Assess the background quality.
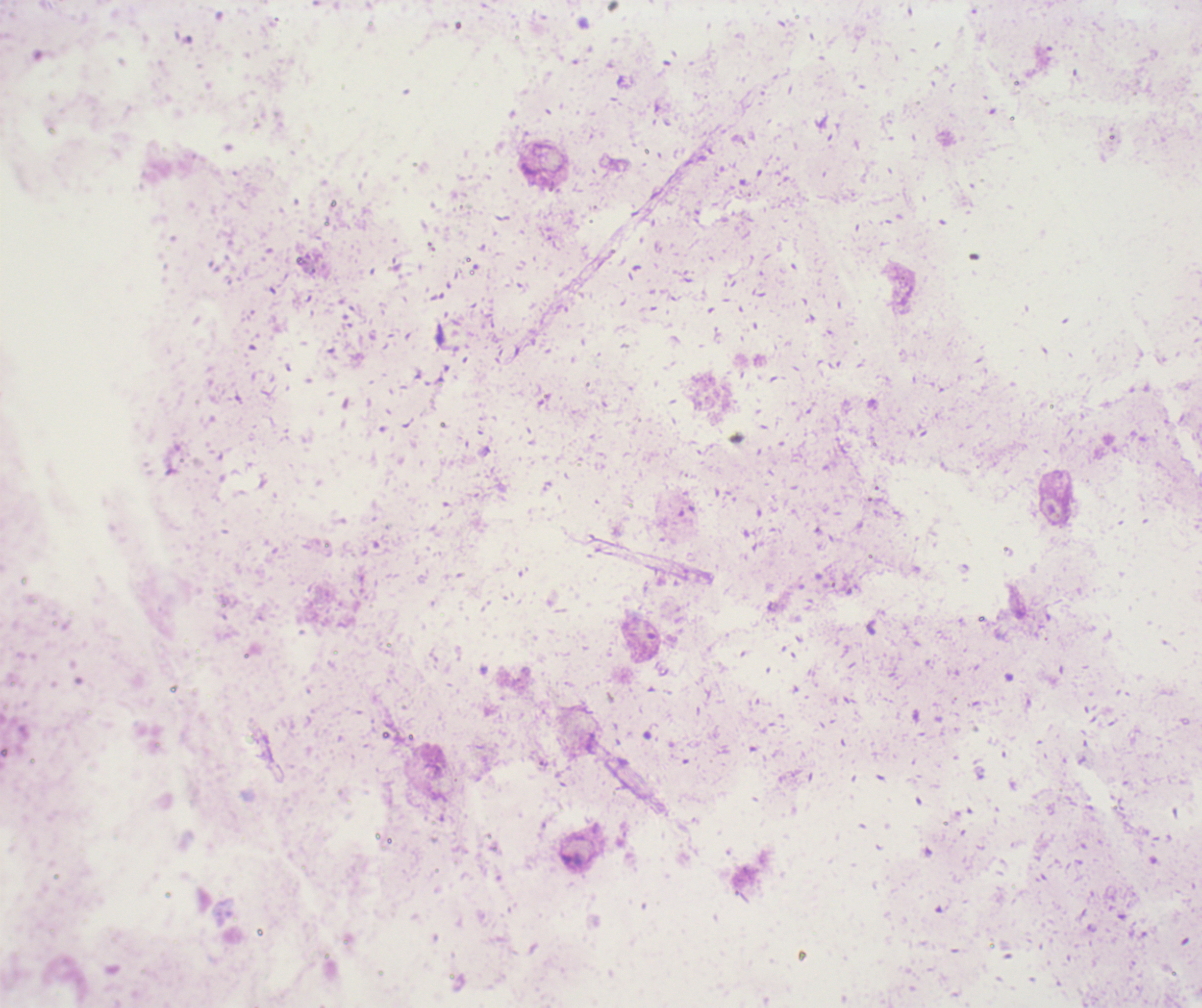

Unsatisfactory.

Approximate centers as (x, y) in pixels. Trophozoite locations: (644, 633). Coloration quality: bad. Previously used in a real diagnosis. Thick smear of blood. Romanowsky stain. Leukocytes: none visible. Single field of view. Image is 1202×1008 pixels. Result: Plasmodium parasites identified. Captured at 100x magnification.